Assess this cell for malaria.
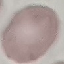

It is uninfected.

Summary:
  - Preparation: thin blood film
  - Capture: smartphone camera at the microscope eyepiece
  - Image type: cell patch, automatically extracted from a larger field of view and resized to 64 × 64 pixels
  - Stain: Giemsa